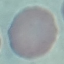
Malaria status: uninfected. Giemsa stain. Automatically extracted cell patch, resized to 64 × 64 pixels. Thin blood smear. Photographed with a smartphone camera at the microscope eyepiece.